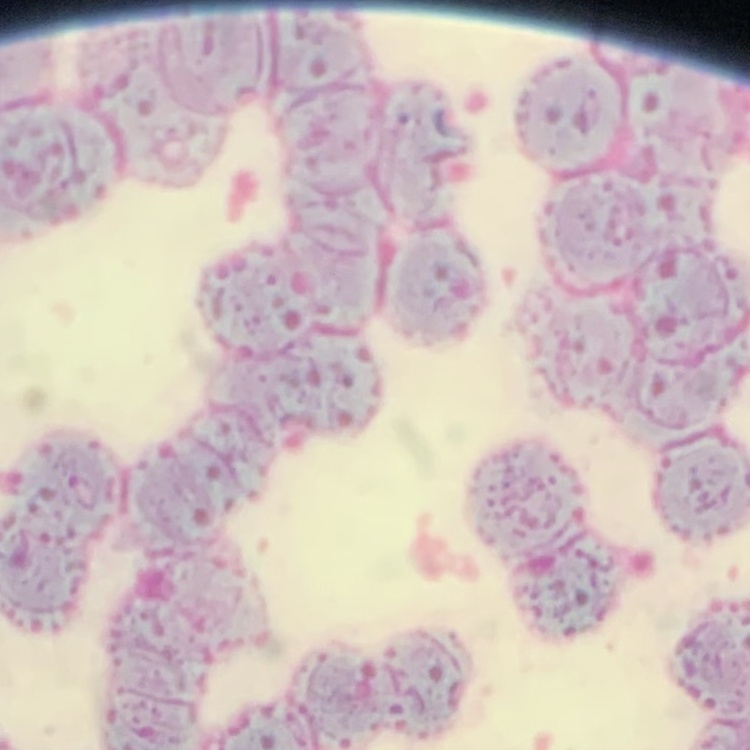 The erythrocytes show rouleaux formation. Thin blood film. One tile cut from a larger photomicrograph. Stained with either Field's or Giemsa.